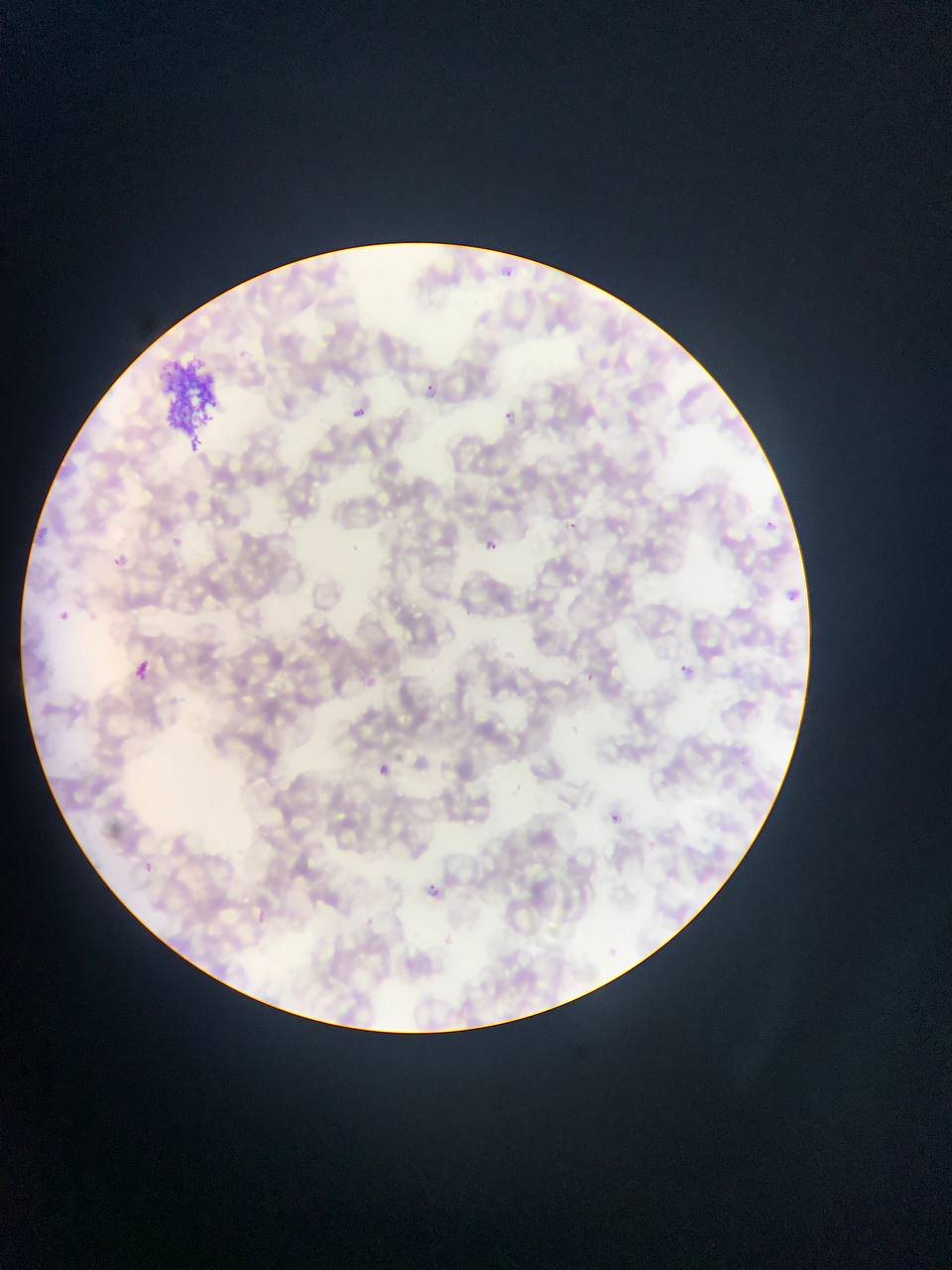

capture = mobile-phone photograph through a microscope
malaria parasite locations = approximate bounding boxes as [left, top, right, bottom] in pixels: [494, 259, 514, 278], [411, 383, 442, 398], [505, 403, 529, 437], [352, 406, 367, 418], [762, 519, 776, 532], [568, 522, 577, 531], [166, 536, 184, 552], [481, 537, 499, 553], [781, 587, 802, 606], [54, 609, 72, 626], [124, 657, 158, 690], [679, 659, 718, 694], [372, 762, 391, 780], [609, 811, 622, 823], [420, 878, 448, 905]
field of view = single
image size = 952×1270 pixels
preparation = thin blood film
country = Ghana
artifact (stain precipitate or debris) locations = approximate bounding boxes as [left, top, right, bottom] in pixels: [153, 352, 236, 451]